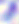
identification = Toxoplasma gondii
magnification = 400x
modality = micrograph